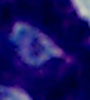
identification: white blood cell
modality: micrograph
magnification: 1000x